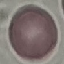

malaria status = uninfected
preparation = thin smear
image type = cell patch, automatically extracted from a larger field of view and resized to 64 × 64 pixels
capture = smartphone camera at the microscope eyepiece
stain = Giemsa